Assess this cell for malaria.
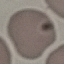

Uninfected.

{
  "capture": "smartphone through the microscope eyepiece",
  "stain": "Giemsa",
  "preparation": "thin blood film",
  "image_type": "cell patch, automatically extracted from a larger field of view and resized to 64 × 64 pixels"
}